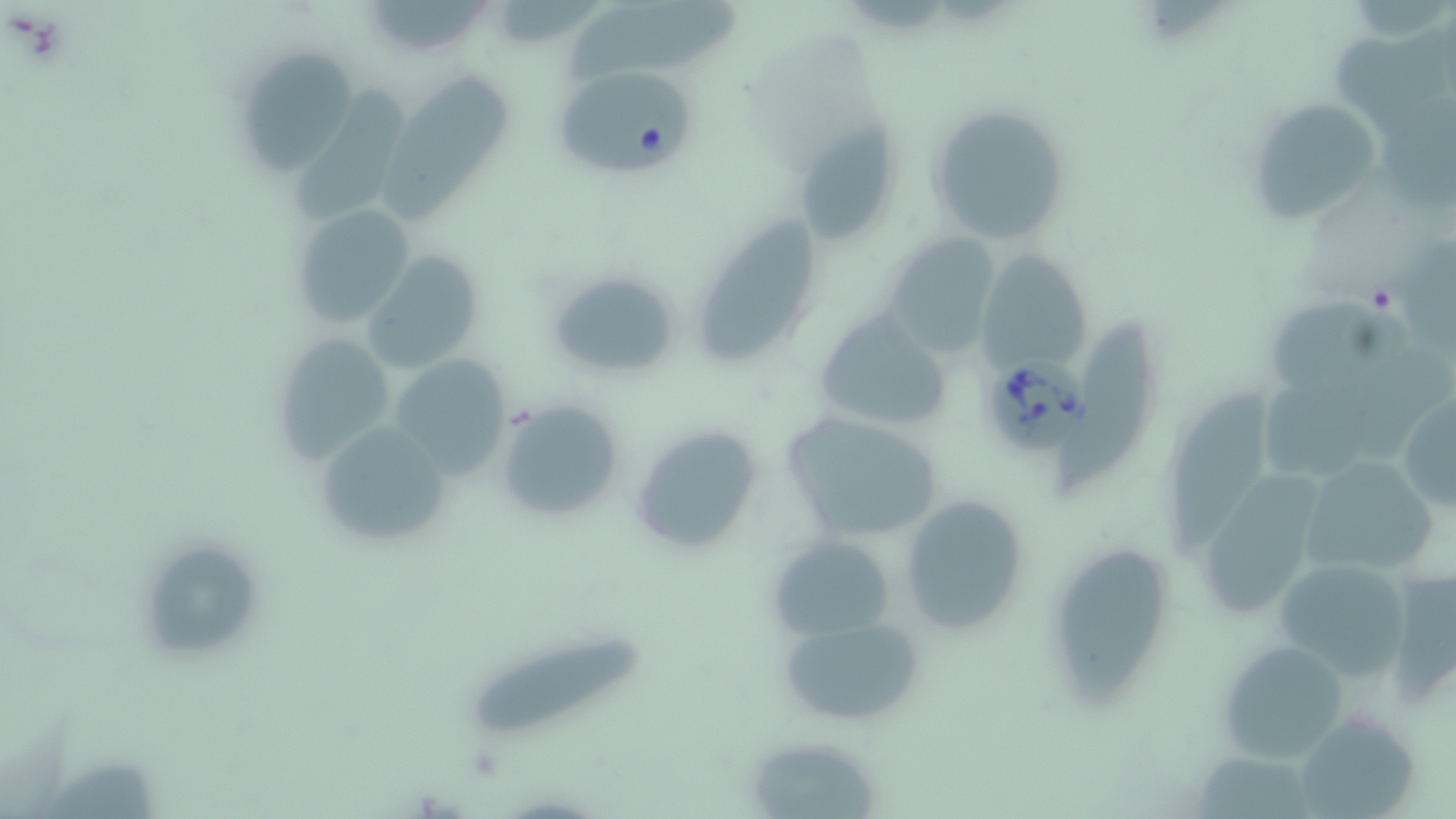
Summary:
  - Coordinate format: approximate bounding boxes as named x1/y1/x2/y2 corners in pixels
  - Uninfected red blood cell locations: (x1=359, y1=0, x2=496, y2=60), (x1=569, y1=0, x2=746, y2=80), (x1=231, y1=45, x2=364, y2=178), (x1=386, y1=71, x2=513, y2=222), (x1=285, y1=85, x2=410, y2=215), (x1=1245, y1=96, x2=1389, y2=228), (x1=927, y1=101, x2=1075, y2=245), (x1=795, y1=123, x2=901, y2=245), (x1=290, y1=202, x2=416, y2=331), (x1=695, y1=211, x2=817, y2=364), (x1=881, y1=233, x2=1000, y2=356), (x1=976, y1=248, x2=1094, y2=378), (x1=362, y1=251, x2=486, y2=376), (x1=544, y1=269, x2=679, y2=383), (x1=1267, y1=297, x2=1413, y2=390), (x1=813, y1=308, x2=956, y2=436), (x1=1066, y1=314, x2=1147, y2=485), (x1=269, y1=330, x2=399, y2=466), (x1=389, y1=353, x2=516, y2=480), (x1=1176, y1=388, x2=1270, y2=558), (x1=1395, y1=393, x2=1456, y2=516), (x1=494, y1=397, x2=624, y2=524), (x1=780, y1=412, x2=943, y2=543), (x1=314, y1=418, x2=454, y2=553), (x1=630, y1=424, x2=765, y2=558), (x1=1297, y1=454, x2=1446, y2=578), (x1=1200, y1=471, x2=1322, y2=619), (x1=898, y1=492, x2=1030, y2=636), (x1=768, y1=534, x2=895, y2=640), (x1=1058, y1=546, x2=1167, y2=709), (x1=148, y1=548, x2=261, y2=657), (x1=1271, y1=559, x2=1412, y2=682), (x1=776, y1=615, x2=927, y2=731), (x1=472, y1=638, x2=642, y2=741), (x1=1215, y1=638, x2=1354, y2=766), (x1=1307, y1=707, x2=1422, y2=819), (x1=752, y1=747, x2=877, y2=819), (x1=1197, y1=750, x2=1315, y2=817), (x1=41, y1=761, x2=159, y2=819)
  - Babesia divergens-infected red blood cell locations: (x1=552, y1=64, x2=695, y2=175), (x1=986, y1=351, x2=1094, y2=455)
  - Slide-level diagnosis: Babesia divergens
  - Preparation: thin blood film
  - Magnification: 1000x
  - Stain: May-Grünwald-Giemsa
  - Image size: 1456×819 pixels
  - Field of view: single
  - Modality: optical microscopy